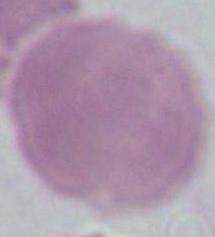

magnification = 1000x
modality = photomicrograph
identification = red blood cell